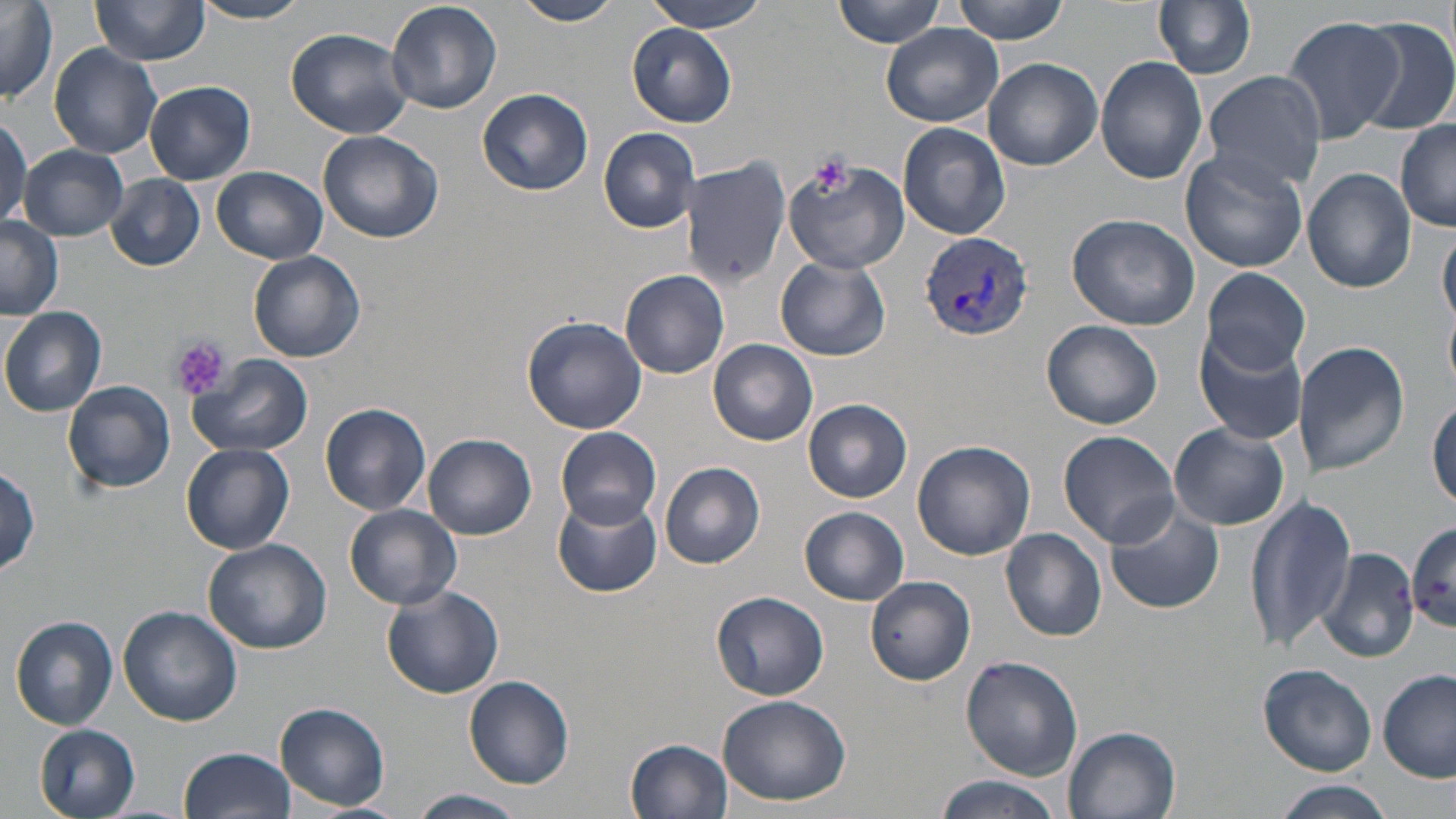
Approximate bounding boxes as (x1, y1, x2, y2) in pixels. Platelet locations: (808, 152, 851, 195), (167, 337, 229, 400). Uninfected red blood cell locations: (89, 0, 211, 66), (514, 0, 621, 25), (646, 0, 770, 33), (832, 0, 948, 48), (953, 0, 1070, 42), (1154, 0, 1257, 80), (191, 1, 312, 24), (385, 1, 501, 114), (0, 2, 59, 104), (1281, 16, 1402, 144), (1351, 17, 1456, 136), (882, 24, 1003, 128), (627, 26, 737, 127), (286, 28, 413, 138), (49, 43, 162, 158), (1096, 56, 1208, 183), (983, 59, 1103, 170), (1204, 72, 1325, 191), (146, 79, 255, 184), (479, 88, 594, 196), (0, 116, 30, 227), (1395, 122, 1456, 231), (897, 123, 1010, 239), (599, 127, 700, 233), (318, 129, 444, 244), (20, 145, 129, 240), (1182, 149, 1309, 275), (680, 154, 792, 288), (782, 156, 909, 274), (21, 161, 202, 258), (210, 165, 327, 265), (1302, 169, 1415, 294), (105, 174, 206, 271), (1067, 210, 1202, 331), (0, 217, 63, 322), (1439, 227, 1456, 326), (248, 250, 366, 364), (776, 256, 891, 362), (1202, 267, 1310, 376), (621, 269, 730, 379), (0, 307, 107, 416), (523, 316, 647, 432), (1041, 320, 1164, 430), (1194, 330, 1306, 444), (709, 339, 818, 446), (1295, 341, 1411, 479), (188, 354, 312, 459), (63, 379, 177, 494), (804, 399, 911, 503), (1429, 400, 1456, 508), (320, 402, 432, 516), (1169, 423, 1288, 530), (556, 426, 662, 528), (1059, 431, 1180, 547), (425, 434, 536, 541), (912, 440, 1035, 559), (181, 444, 294, 554), (661, 461, 768, 569), (0, 466, 44, 577), (551, 492, 662, 597), (1245, 498, 1355, 652), (1105, 503, 1225, 614), (343, 504, 462, 610), (799, 507, 910, 604), (1407, 522, 1456, 632), (1000, 528, 1108, 641), (204, 539, 331, 655), (1317, 546, 1420, 661), (865, 577, 974, 686), (380, 583, 506, 698), (711, 591, 830, 701), (119, 606, 242, 726), (10, 616, 119, 730), (960, 656, 1083, 779), (1259, 663, 1378, 777), (1379, 669, 1455, 782), (463, 674, 575, 789), (719, 693, 852, 806), (275, 702, 390, 813), (35, 724, 141, 818), (1064, 726, 1182, 819), (625, 737, 733, 818), (182, 747, 296, 819), (933, 776, 1062, 819), (1271, 780, 1397, 818), (410, 789, 527, 819), (299, 803, 407, 819). Plasmodium vivax-infected red blood cell locations: (919, 232, 1033, 344). Slide-level diagnosis: Plasmodium vivax. Captured at 1000x magnification. One field of a larger specimen. Thin blood smear. Light microscopy. Image is 1456×819 pixels. May-Grünwald-Giemsa-stained preparation.